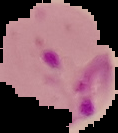

Summary:
  - Preparation: thin blood film
  - Result: malaria parasites identified
  - Image size: 118×133 pixels
  - Image type: cell region segmented out of the field of view; surrounding area masked to black